Comment on the morphology of the erythrocytes.
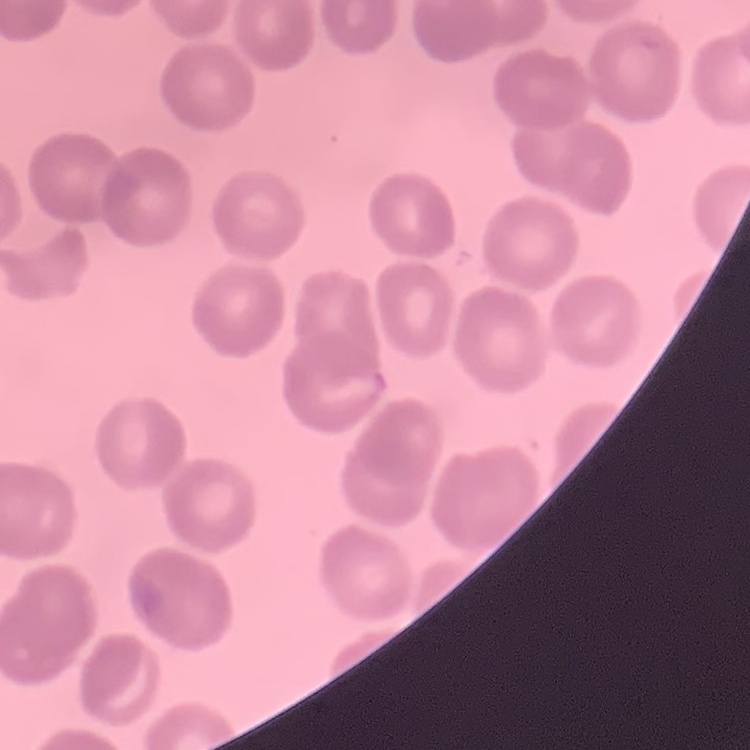

No rouleaux formation.

Square crop of a larger photomicrograph. Stained with either Field's or Giemsa. Thin blood film.